Locate every blood parasite and identify its species.
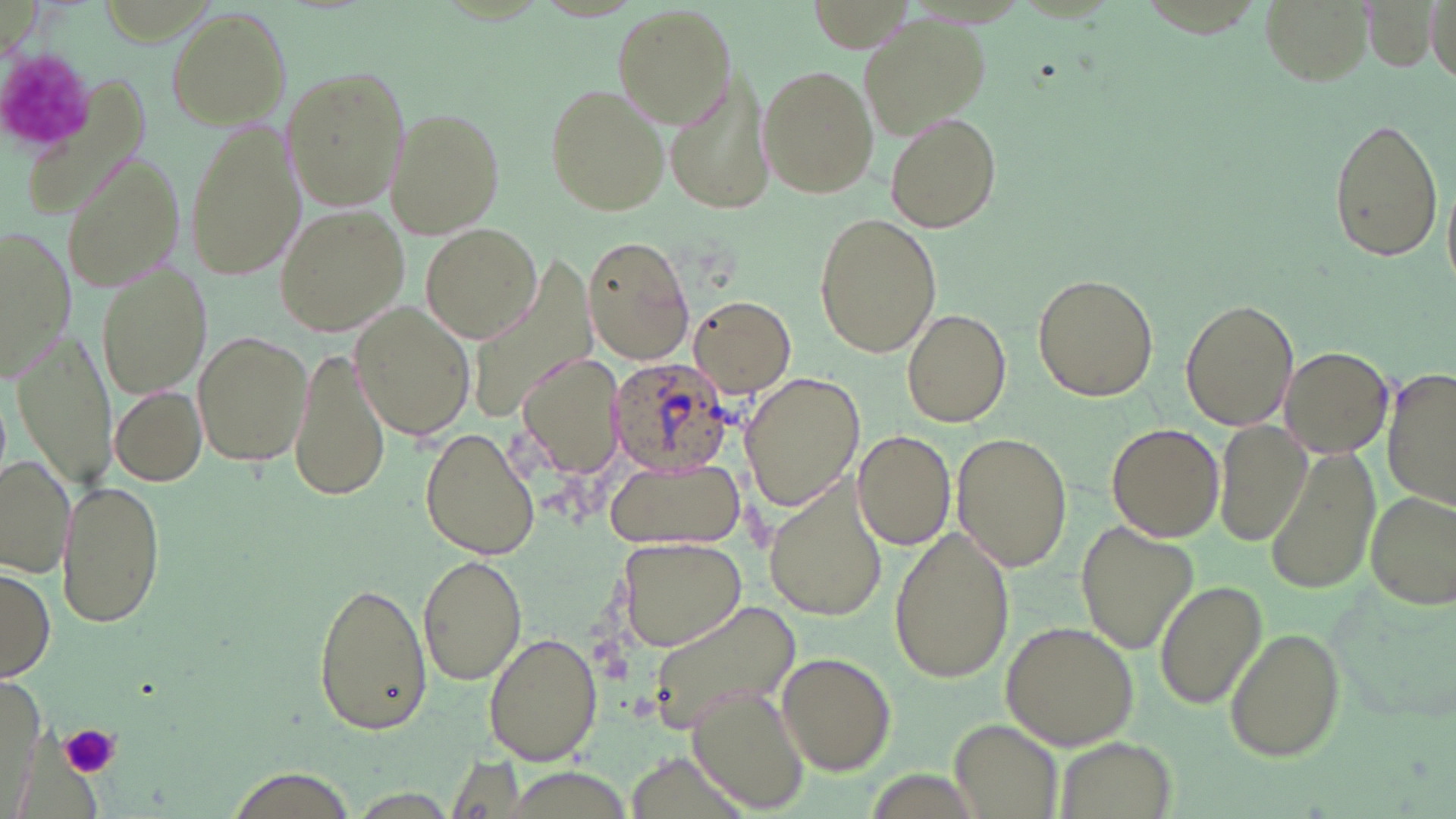
Approximate bounding boxes as (x1,y1)-(x2,y2) corner pairs in pixels.
Plasmodium ovale-infected red blood cells: (606,357)-(736,477).
No Plasmodium falciparum, Plasmodium malariae, Plasmodium vivax, Babesia divergens, or Trypanosoma brucei observed.

Uninfected red blood cell locations: (612,4)-(737,129), (163,6)-(292,131), (861,11)-(991,137), (757,63)-(879,200), (281,65)-(408,213), (665,73)-(770,216), (545,83)-(669,215), (383,108)-(508,239), (885,113)-(1002,233), (1327,115)-(1443,262), (184,119)-(303,283), (59,152)-(186,295), (273,205)-(410,338), (813,212)-(943,360), (0,222)-(76,380), (422,224)-(542,343), (582,235)-(693,363), (93,261)-(213,399), (1030,272)-(1160,404), (688,295)-(796,395), (1180,297)-(1299,433), (349,303)-(476,442), (902,307)-(1012,428), (192,329)-(313,469), (12,331)-(117,494), (287,343)-(392,504), (1278,347)-(1393,459), (516,352)-(627,483), (1382,367)-(1456,511), (740,371)-(864,512), (109,385)-(208,486), (1214,419)-(1314,550), (1105,422)-(1224,543), (419,427)-(542,560), (852,430)-(955,551), (952,433)-(1071,572), (1265,447)-(1383,596), (0,451)-(77,576), (606,457)-(744,551), (766,476)-(891,621), (55,478)-(166,629), (1367,490)-(1454,607), (1075,521)-(1197,654), (888,522)-(1015,684), (616,537)-(749,653), (416,553)-(525,685), (1,562)-(54,685), (310,579)-(432,736), (1155,580)-(1265,711), (644,597)-(801,735), (1003,620)-(1139,752), (1224,628)-(1346,763), (482,634)-(604,769), (776,651)-(896,773), (686,685)-(812,813), (949,720)-(1063,819), (1052,734)-(1175,819), (220,767)-(361,819). Platelet locations: (61,724)-(121,780). Slide-level diagnosis: Plasmodium ovale. May-Grünwald-Giemsa stain. Light microscopy. Thin blood film. Single field of view. Captured at 1000x magnification. Image is 1456×819 pixels.